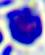

Summary:
  - Identification: leukocyte
  - Modality: photomicrograph
  - Magnification: 400x